Identify the parasite.
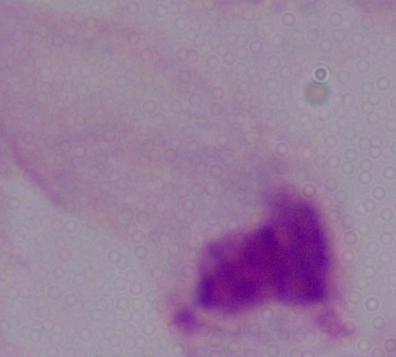

This is a trichomonad.

Captured at 1000x magnification. Micrograph.